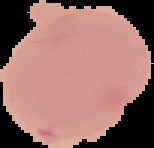

Cell region segmented out of the field of view; the surrounding area is masked to black. Result: no malaria parasites detected. Image is 154×148 pixels. From a thin blood smear.